Give the position of every Plasmodium parasite.
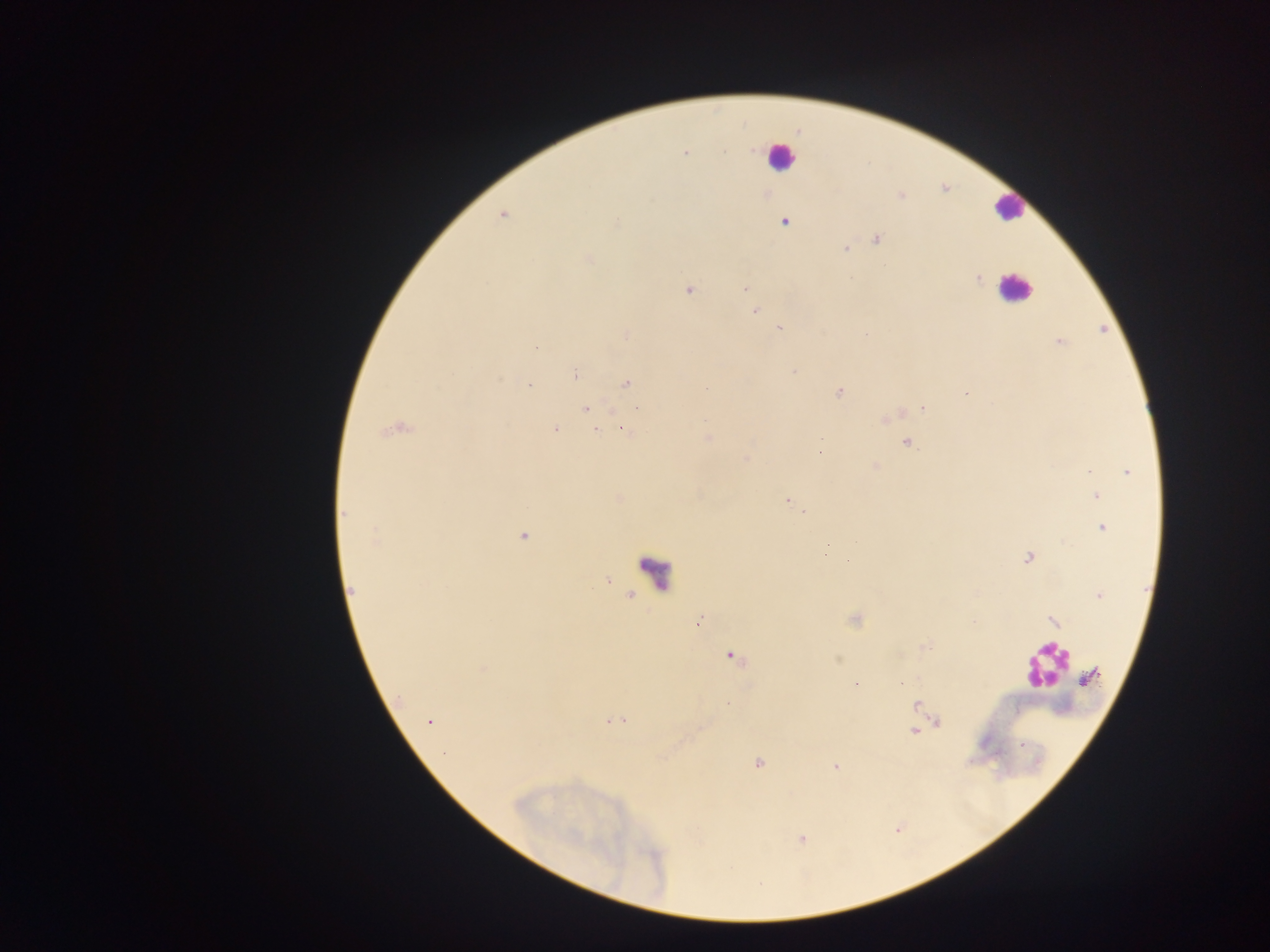

Approximate centers as {x, y} in pixels.
Plasmodium parasites: {752, 149}, {723, 151}, {685, 152}, {901, 195}, {503, 215}, {617, 221}, {784, 222}, {876, 239}, {845, 249}, {589, 259}, {978, 279}, {745, 288}, {688, 290}, {755, 310}, {780, 327}, {865, 334}, {626, 335}, {1059, 342}, {536, 348}, {794, 371}, {576, 375}, {626, 384}, {529, 386}, {839, 392}, {965, 393}, {637, 408}, {923, 408}, {585, 409}, {555, 429}, {394, 430}, {596, 431}, {625, 431}, {708, 437}, {820, 438}, {907, 442}, {819, 452}, {745, 459}, {876, 467}, {1089, 470}, {1127, 473}, {1097, 496}, {788, 500}, {804, 512}, {344, 513}, {1102, 527}, {523, 537}, {376, 539}, {855, 542}, {827, 548}, {1028, 558}, {847, 561}, {352, 589}, {1098, 596}, {698, 622}, {1053, 622}, {732, 655}, {484, 667}, {1089, 677}, {901, 683}, {856, 684}, {728, 704}, {916, 706}, {615, 720}, {429, 722}, {936, 722}, {914, 732}, {758, 764}, {836, 767}, {803, 839}.

Summary:
  - Leukocyte locations: {779, 156}, {1008, 207}, {1014, 288}, {657, 567}, {1043, 667}
  - Field of view: single
  - Capture: mobile-phone photograph through a microscope
  - Image size: 1270×952 pixels
  - Preparation: thick blood film
  - Country: Ghana